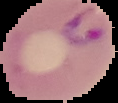
Malaria status: parasitized. Segmented cell region on a black background. From a thin blood film. Image is 118×103 pixels.